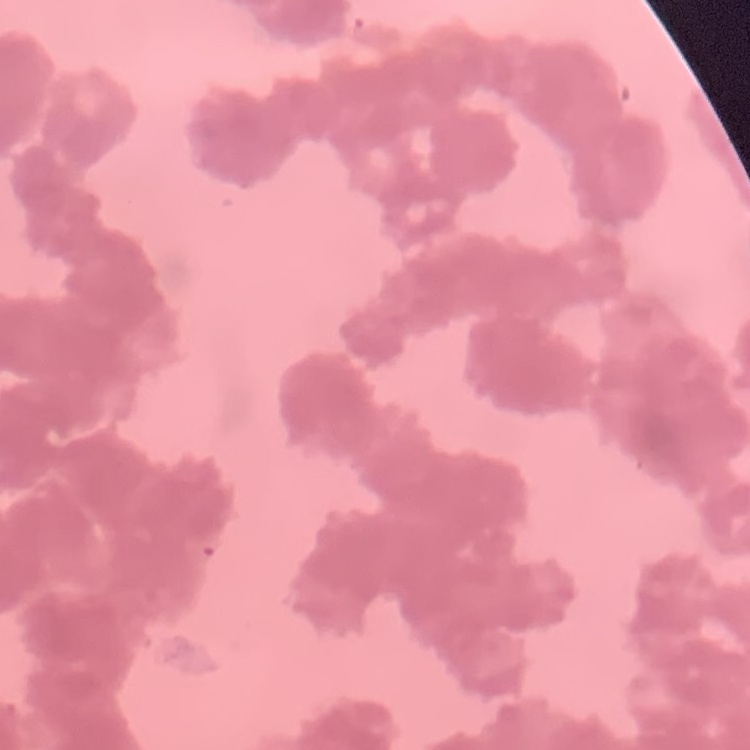
{
  "erythrocyte_morphology": "rouleaux formation",
  "image_type": "square crop of a larger photomicrograph",
  "stain": "Field's or Giemsa",
  "preparation": "thin blood film"
}